Identify the parasite.
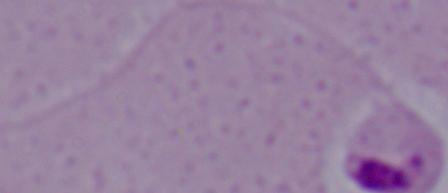
Leishmania.

magnification = 1000x
modality = photomicrograph